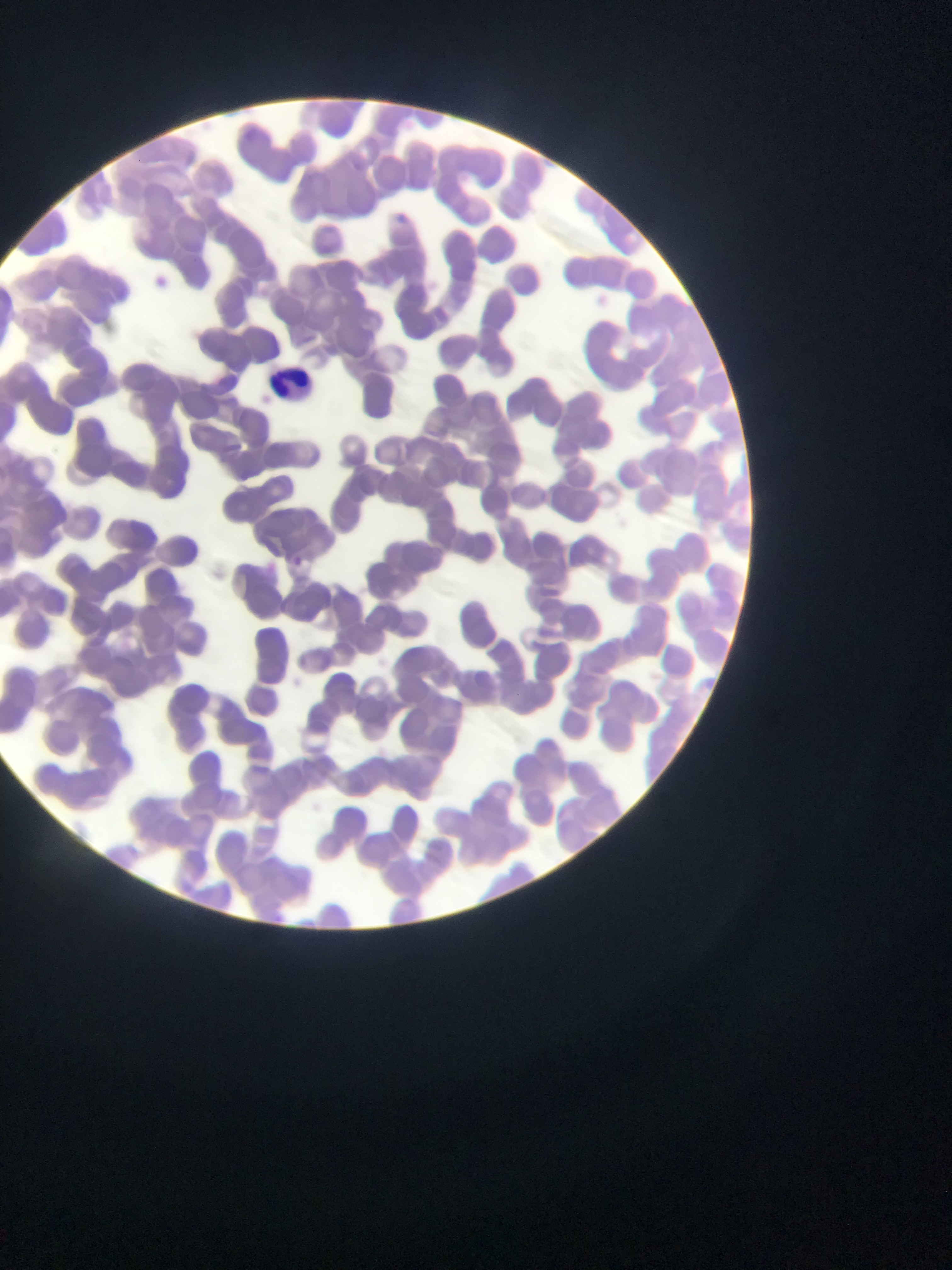
image size = 952×1270 pixels
preparation = thin blood film
capture = mobile-phone photograph through a microscope
country = Ghana
leukocyte locations = approximate bounding boxes as {left, top, right, bottom} in pixels: {266, 354, 320, 394}
malaria parasite locations = approximate bounding boxes as {left, top, right, bottom} in pixels: {397, 209, 409, 222}, {153, 272, 174, 288}, {293, 556, 304, 569}
field of view = single